Identify the cell.
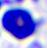

A leukocyte.

Photomicrograph. 400x magnification.